Assess the morphology of the red blood cells.
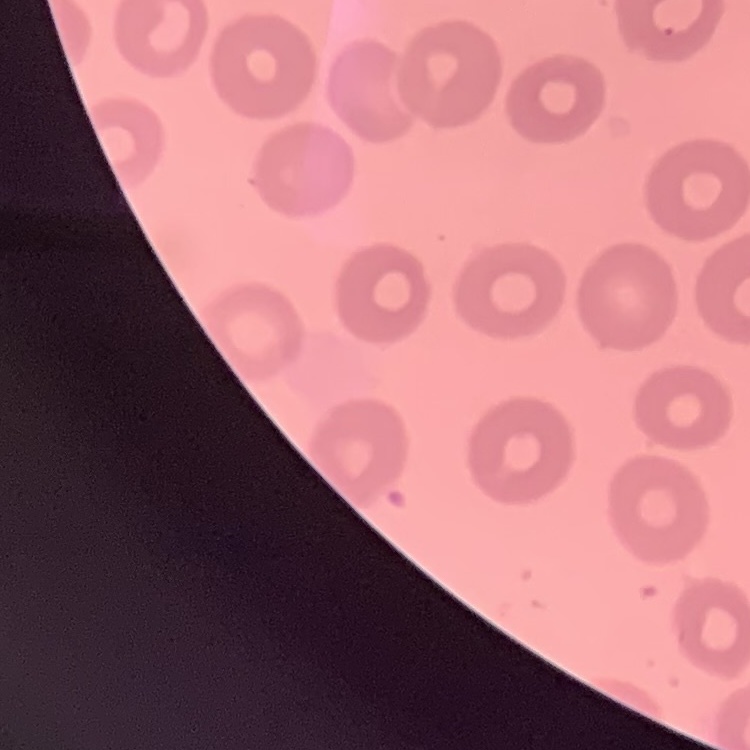
They show no rouleaux formation.

preparation: thin peripheral smear
image_type: one tile cut from a larger photomicrograph
stain: Field's or Giemsa